Give the extent of all Plasmodium falciparum-infected red blood cells.
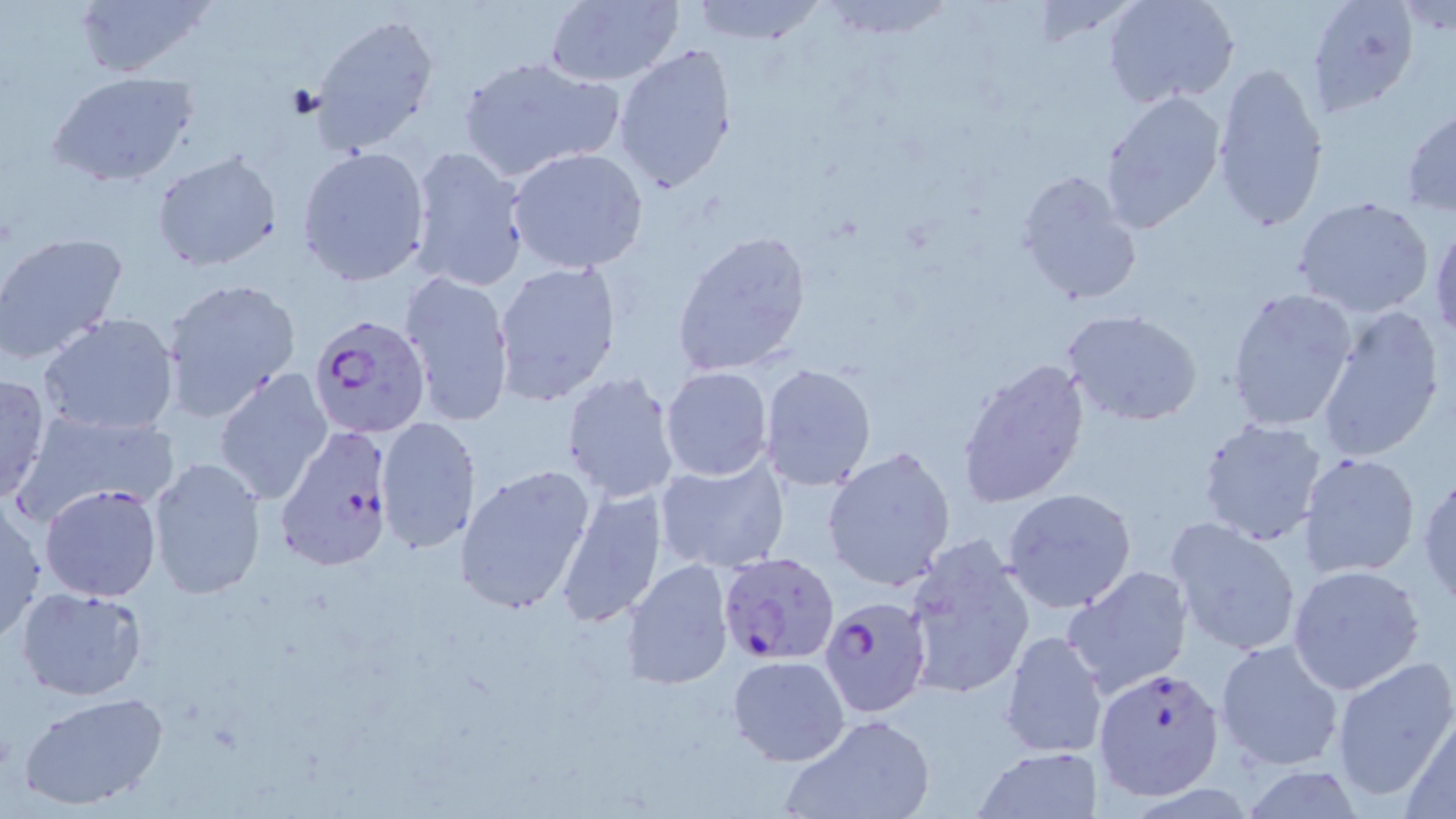

Approximate bounding boxes as (x1,y1)-(x2,y2) corner pairs in pixels.
Plasmodium falciparum-infected red blood cells: (309,312)-(434,439), (276,425)-(397,572), (717,554)-(840,663), (820,596)-(934,721), (1093,663)-(1225,801).

slide-level diagnosis = Plasmodium falciparum
image size = 1456×819 pixels
field of view = one of a larger specimen
magnification = 1000x
modality = optical microscopy
preparation = thin blood film
uninfected red blood cell locations = approximate bounding boxes as (x1,y1)-(x2,y2) corner pairs in pixels: (69,0)-(217,80), (541,0)-(684,87), (685,0)-(827,45), (820,0)-(955,40), (1306,0)-(1421,117), (1104,1)-(1241,108), (1393,3)-(1456,37), (309,12)-(440,155), (613,42)-(739,195), (457,53)-(625,182), (1210,62)-(1329,235), (49,71)-(198,188), (1098,90)-(1226,235), (1401,106)-(1456,216), (407,145)-(531,293), (297,147)-(432,287), (505,147)-(650,276), (151,150)-(282,273), (1015,169)-(1143,307), (1292,195)-(1436,318), (1429,217)-(1456,339), (672,230)-(814,379), (0,231)-(129,365), (493,260)-(622,405), (397,271)-(515,426), (160,276)-(302,421), (1224,286)-(1359,432), (1315,303)-(1448,462), (1063,310)-(1204,427), (38,312)-(182,437), (954,355)-(1091,510), (758,365)-(876,490), (661,366)-(773,481), (215,368)-(334,506), (560,370)-(680,504), (0,373)-(52,504), (14,408)-(179,520), (375,416)-(480,555), (1196,416)-(1328,545), (822,446)-(956,592), (1298,450)-(1421,579), (147,457)-(268,599), (654,457)-(788,573), (455,464)-(596,616), (1415,470)-(1456,605), (39,483)-(164,602), (555,485)-(667,628), (1003,488)-(1137,614), (0,498)-(47,642), (1164,516)-(1304,657), (901,534)-(1037,703), (625,560)-(735,688), (1286,564)-(1427,695), (1063,567)-(1192,696), (16,587)-(149,700), (999,629)-(1108,760), (1214,639)-(1345,771), (727,654)-(851,767), (1331,655)-(1456,803), (18,691)-(170,812), (780,712)-(939,819), (1400,712)-(1456,818), (973,747)-(1103,817)
stain = May-Grünwald-Giemsa